Classify this cell by malaria status.
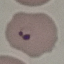
It is parasitized.

Summary:
  - Stain: Giemsa
  - Capture: smartphone through the microscope eyepiece
  - Preparation: thin blood film
  - Image type: cell patch, automatically extracted from a larger field of view and resized to 64 × 64 pixels